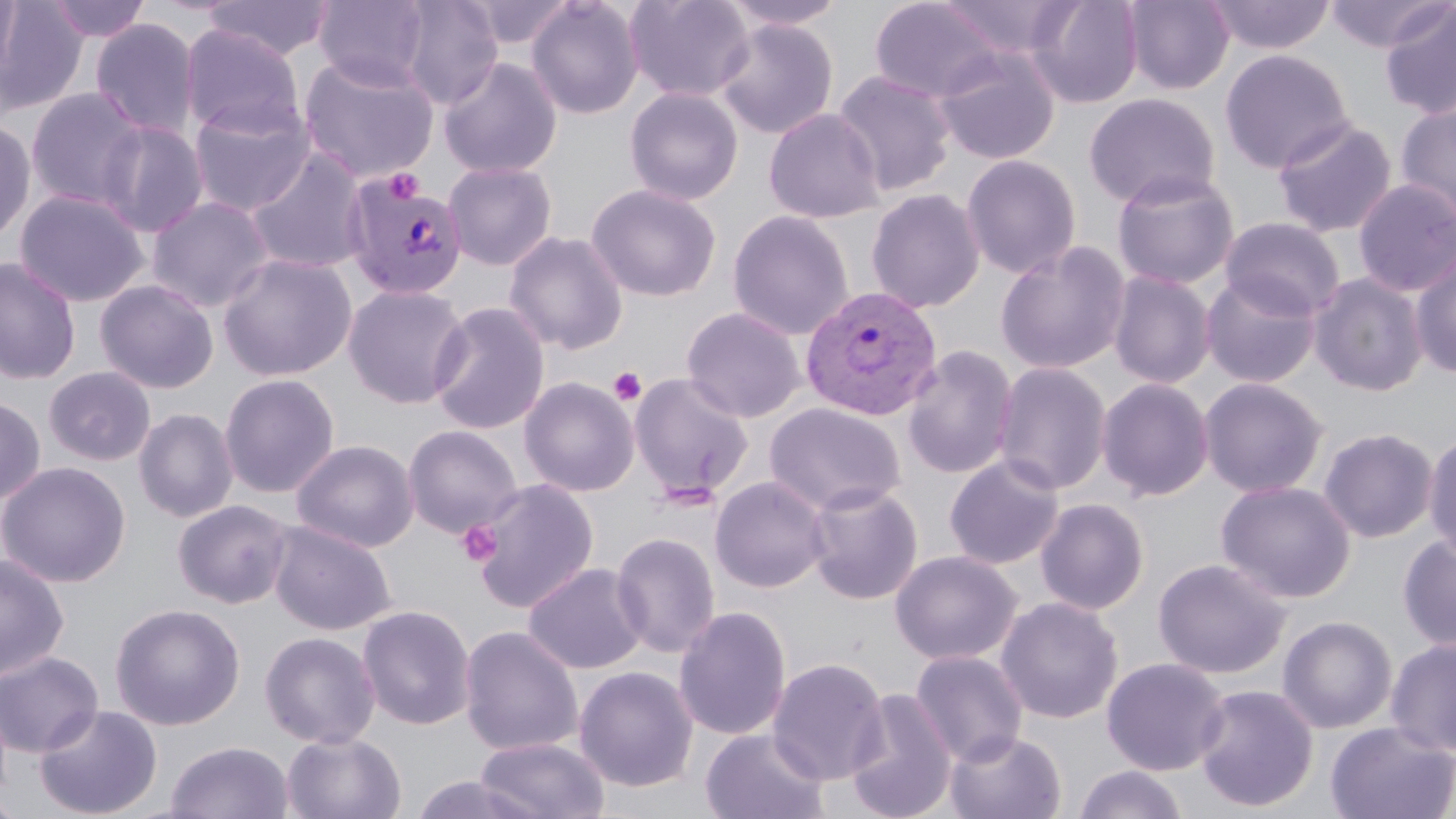

Summary:
  - Coordinate format: approximate bounding boxes as (x1,y1)-(x2,y2) corner pairs in pixels
  - Platelet locations: (383,169)-(424,203), (608,367)-(647,406), (458,521)-(502,566)
  - Plasmodium vivax-infected red blood cell locations: (342,172)-(469,301), (800,285)-(943,421)
  - Uninfected red blood cell locations: (0,0)-(20,83), (45,0)-(152,42), (314,0)-(431,89), (394,0)-(504,109), (526,0)-(645,119), (623,0)-(755,102), (718,0)-(851,30), (869,0)-(1006,103), (934,0)-(1083,60), (1026,0)-(1144,109), (1122,0)-(1235,96), (1204,0)-(1336,55), (1324,0)-(1452,55), (0,1)-(89,116), (201,1)-(333,61), (464,1)-(576,51), (1379,3)-(1456,121), (90,18)-(199,138), (714,18)-(839,140), (180,24)-(304,137), (933,44)-(1061,165), (1220,50)-(1355,174), (298,53)-(440,183), (438,56)-(563,179), (832,69)-(957,197), (624,86)-(744,206), (26,87)-(148,211), (1083,93)-(1221,209), (187,98)-(316,217), (1395,101)-(1456,228), (764,108)-(885,223), (1272,116)-(1398,237), (0,117)-(36,246), (97,120)-(209,237), (245,147)-(371,274), (960,153)-(1082,279), (443,161)-(558,271), (1111,170)-(1241,290), (1352,178)-(1456,297), (585,182)-(722,302), (865,187)-(986,314), (15,189)-(149,307), (147,196)-(274,313), (727,210)-(853,340), (1220,216)-(1347,321), (503,231)-(629,355), (995,240)-(1132,375), (1410,249)-(1456,379), (218,252)-(357,381), (0,257)-(81,386), (1107,270)-(1216,389), (1200,272)-(1322,389), (1308,273)-(1429,397), (95,279)-(219,394), (342,284)-(471,409), (428,301)-(550,435), (681,306)-(807,423), (901,345)-(1019,480), (992,361)-(1112,496), (43,366)-(156,466), (628,371)-(755,503), (219,373)-(340,498), (518,376)-(640,497), (1096,377)-(1215,501), (1198,377)-(1329,498), (0,396)-(46,505), (765,402)-(906,515), (133,408)-(239,523), (403,424)-(523,538), (1318,427)-(1439,543), (1424,430)-(1456,563), (291,439)-(419,552), (943,454)-(1065,570), (0,461)-(131,587), (709,476)-(831,593), (470,478)-(600,614), (1216,480)-(1357,603), (804,482)-(924,605), (1035,497)-(1150,615), (173,499)-(293,608), (268,520)-(396,635), (610,531)-(721,658), (1397,533)-(1456,652), (890,550)-(1022,665), (0,552)-(70,682), (1152,557)-(1291,679), (523,562)-(649,675), (995,597)-(1124,724), (109,602)-(246,730), (357,604)-(476,731), (674,604)-(792,741), (1277,615)-(1397,734), (459,625)-(584,756), (260,630)-(381,749), (1385,636)-(1456,757), (0,650)-(104,757), (910,650)-(1029,765), (767,656)-(889,785), (1101,657)-(1231,776), (574,666)-(698,792), (1193,683)-(1320,812), (843,688)-(958,819), (32,703)-(163,819), (1325,721)-(1456,819), (701,726)-(830,819), (281,730)-(407,819), (945,730)-(1067,819), (474,736)-(611,819), (166,740)-(293,819), (1073,764)-(1190,819), (409,774)-(544,819), (0,792)-(24,819)
  - Slide-level diagnosis: Plasmodium vivax
  - Magnification: 1000x
  - Preparation: thin blood film
  - Modality: optical microscopy
  - Image size: 1456×819 pixels
  - Stain: May-Grünwald-Giemsa
  - Field of view: one of a larger specimen